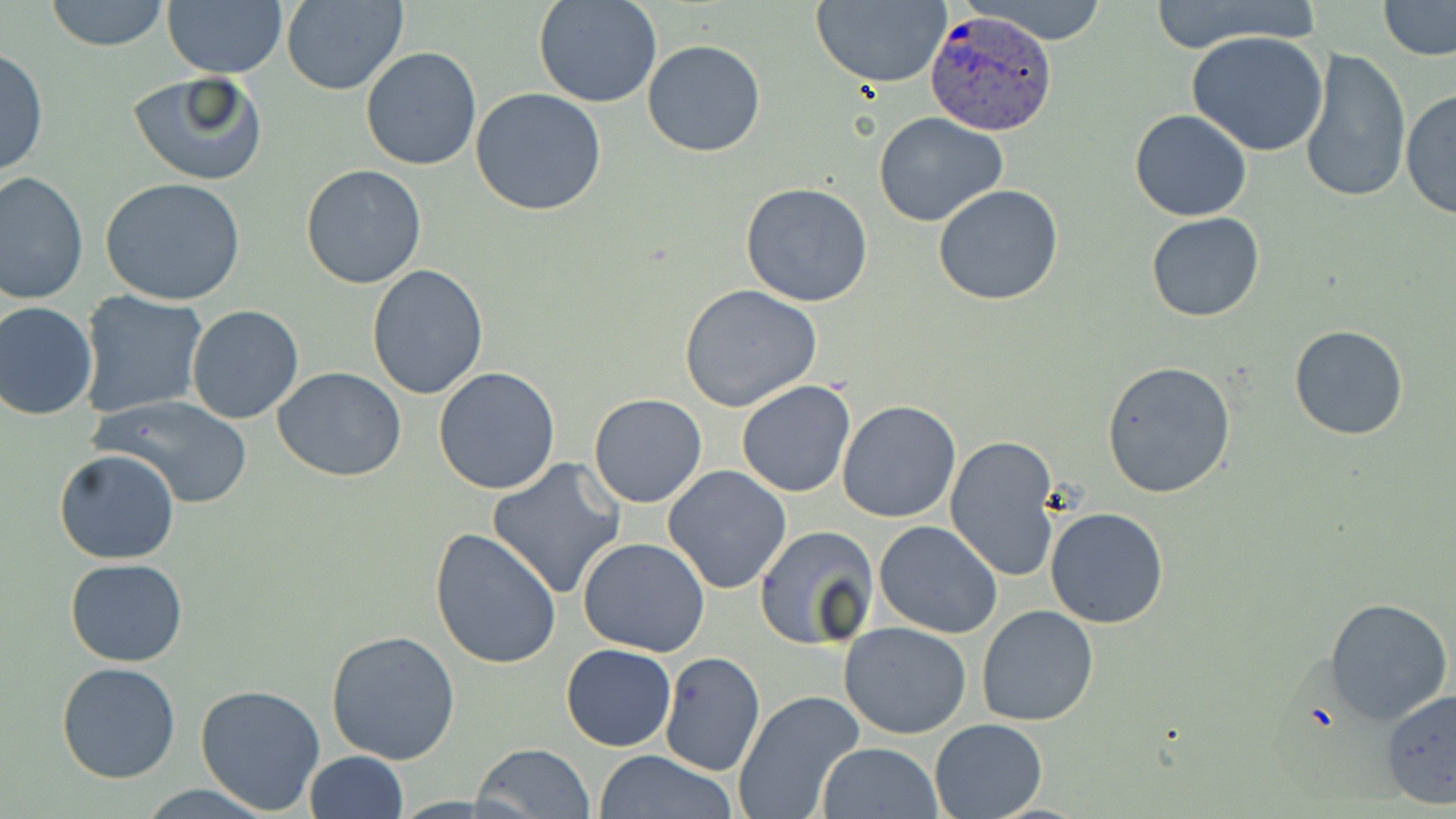

Approximate bounding boxes as named x1/y1/x2/y2 corners in pixels. Plasmodium ovale-infected red blood cell locations: (x1=926, y1=10, x2=1055, y2=135). Uninfected red blood cell locations: (x1=44, y1=0, x2=170, y2=51), (x1=533, y1=0, x2=662, y2=108), (x1=812, y1=0, x2=952, y2=88), (x1=958, y1=0, x2=1115, y2=45), (x1=1142, y1=0, x2=1325, y2=55), (x1=1378, y1=0, x2=1456, y2=60), (x1=161, y1=1, x2=288, y2=78), (x1=279, y1=1, x2=409, y2=94), (x1=1188, y1=32, x2=1331, y2=157), (x1=641, y1=39, x2=766, y2=157), (x1=1299, y1=44, x2=1410, y2=206), (x1=1, y1=46, x2=48, y2=180), (x1=360, y1=46, x2=484, y2=171), (x1=127, y1=71, x2=267, y2=185), (x1=470, y1=87, x2=606, y2=216), (x1=1400, y1=87, x2=1456, y2=220), (x1=1130, y1=108, x2=1252, y2=222), (x1=873, y1=111, x2=1008, y2=227), (x1=300, y1=164, x2=427, y2=288), (x1=0, y1=173, x2=88, y2=304), (x1=99, y1=177, x2=247, y2=305), (x1=740, y1=181, x2=874, y2=306), (x1=933, y1=183, x2=1063, y2=306), (x1=1146, y1=212, x2=1265, y2=323), (x1=366, y1=263, x2=490, y2=400), (x1=679, y1=285, x2=821, y2=411), (x1=77, y1=292, x2=208, y2=419), (x1=0, y1=301, x2=98, y2=421), (x1=186, y1=304, x2=304, y2=424), (x1=1288, y1=324, x2=1409, y2=440), (x1=1101, y1=360, x2=1236, y2=500), (x1=273, y1=367, x2=407, y2=480), (x1=433, y1=368, x2=561, y2=495), (x1=736, y1=378, x2=855, y2=498), (x1=88, y1=394, x2=257, y2=509), (x1=589, y1=394, x2=707, y2=508), (x1=837, y1=399, x2=962, y2=522), (x1=946, y1=435, x2=1063, y2=584), (x1=54, y1=449, x2=181, y2=564), (x1=486, y1=458, x2=627, y2=599), (x1=661, y1=465, x2=792, y2=594), (x1=1044, y1=507, x2=1170, y2=629), (x1=874, y1=521, x2=1003, y2=639), (x1=753, y1=525, x2=880, y2=649), (x1=429, y1=527, x2=563, y2=671), (x1=577, y1=537, x2=710, y2=658), (x1=65, y1=559, x2=189, y2=668), (x1=1325, y1=596, x2=1453, y2=724), (x1=977, y1=604, x2=1099, y2=726), (x1=839, y1=621, x2=971, y2=738), (x1=326, y1=627, x2=460, y2=765), (x1=559, y1=643, x2=677, y2=751), (x1=660, y1=651, x2=765, y2=777), (x1=57, y1=663, x2=182, y2=783), (x1=195, y1=682, x2=326, y2=814), (x1=1381, y1=688, x2=1456, y2=813), (x1=733, y1=691, x2=864, y2=819), (x1=929, y1=717, x2=1048, y2=817), (x1=816, y1=741, x2=944, y2=819), (x1=472, y1=742, x2=595, y2=819), (x1=593, y1=749, x2=738, y2=819), (x1=303, y1=751, x2=408, y2=819), (x1=135, y1=784, x2=276, y2=818). Slide-level diagnosis: Plasmodium ovale. One field of a larger specimen. May-Grünwald-Giemsa-stained preparation. Thin blood film. Captured at 1000x magnification. Image is 1456×819 pixels. Optical microscopy.